Locate every Plasmodium falciparum parasite and give its life-cycle stage, and locate every leukocyte and any debris.
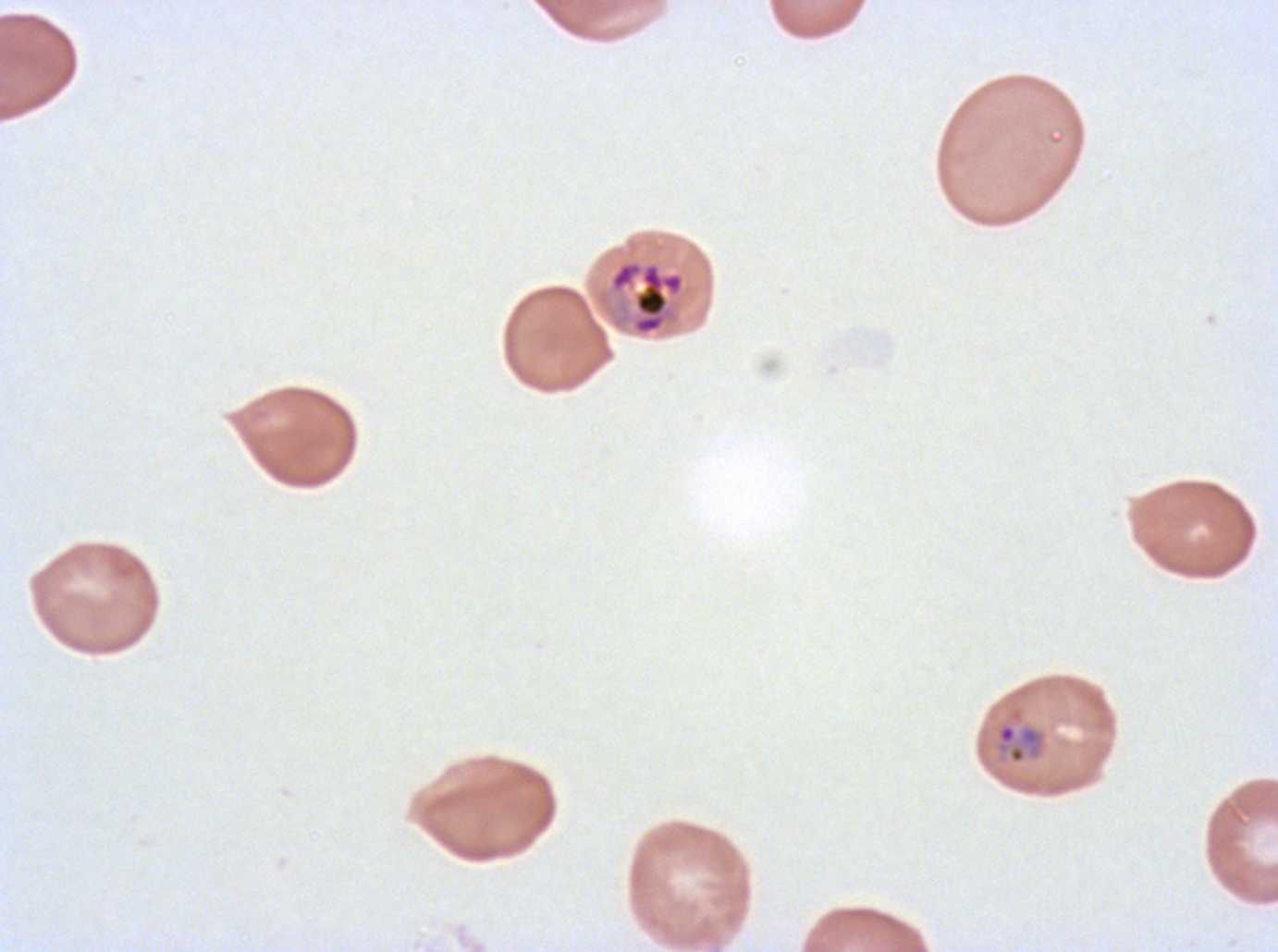
Approximate bounding rectangles given as corner coordinates in pixels from the top-left.
Rings: (x1=994, y1=709, x2=1047, y2=765).
Late trophozoites: (x1=595, y1=258, x2=686, y2=337).
No late-ring/early-trophozoite forms, mid trophozoites, early schizonts, late schizonts, segmenters, gametocytes, leukocytes, or debris observed.

Summary:
  - Stain: Giemsa
  - Specimen: ex-vivo Plasmodium falciparum culture from a patient in The Gambia, grown for 24 to 48 hours
  - Field of view: one sub-image of a larger composite
  - Image size: 1278×952 pixels
  - Preparation: thin blood film
  - Life-cycle stages observed: ring, late trophozoite